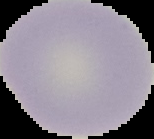

Summary:
  - Preparation: thin blood film
  - Result: no malaria parasites detected
  - Image type: segmented cell region with the area outside set to black
  - Image size: 154×139 pixels